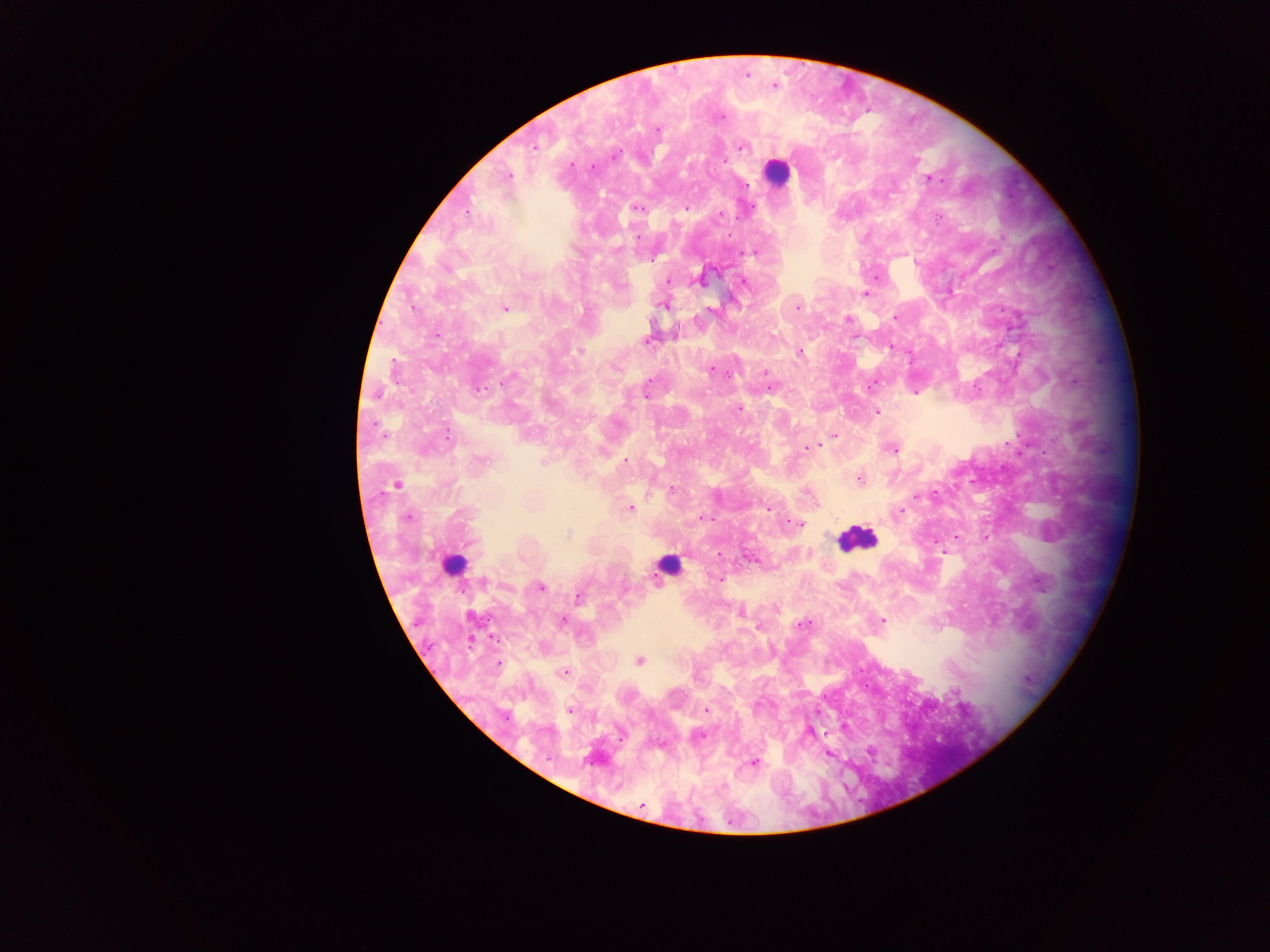
Approximate centers as x y in pixels. Leukocyte locations (subset; some below the resolvable size): 775 173; 856 538; 454 565; 669 566. Plasmodium parasite locations: 774 87; 722 117; 657 129; 535 147; 742 147; 615 156; 726 160; 572 165; 591 167; 508 176; 930 178; 638 207; 686 209; 467 211; 720 215; 937 217; 728 234; 638 236; 749 252; 876 278; 668 281; 699 281; 744 282; 866 294; 663 305; 505 308; 797 308; 711 310; 896 317; 849 319; 437 335; 855 337; 646 341; 891 346; 579 350; 799 352; 711 370; 764 372; 728 375; 507 379; 649 380; 1075 381; 769 387; 870 387; 478 389; 915 393; 646 395; 739 410; 877 412; 835 436; 447 437; 820 445; 807 448; 892 449; 625 460; 484 461; 543 461; 860 479; 397 485; 672 490; 933 493; 917 497; 630 508; 768 508; 901 511; 408 517; 702 517; 798 523; 567 534; 956 536; 986 536; 936 544; 753 561; 720 579; 484 582; 540 587; 578 597; 740 613; 562 620; 882 620; 802 625; 759 626; 493 638; 640 660; 499 664; 564 671; 570 710; 706 710; 506 717; 701 735; 754 763; 641 805. Sample from Ghana. Thick blood film. Mobile-phone photograph taken through the microscope. Image is 1270×952 pixels. Single field of view.